Classify this cell by malaria status.
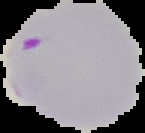

Parasitized.

The area outside the segmented cell region is set to black. Image is 145×133 pixels. From a thin blood film.